Name the cell type shown.
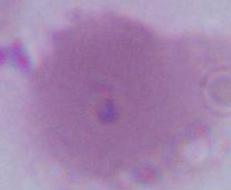
This is an erythrocyte.

Photomicrograph. 1000x magnification.